Look for Plasmodium parasites.
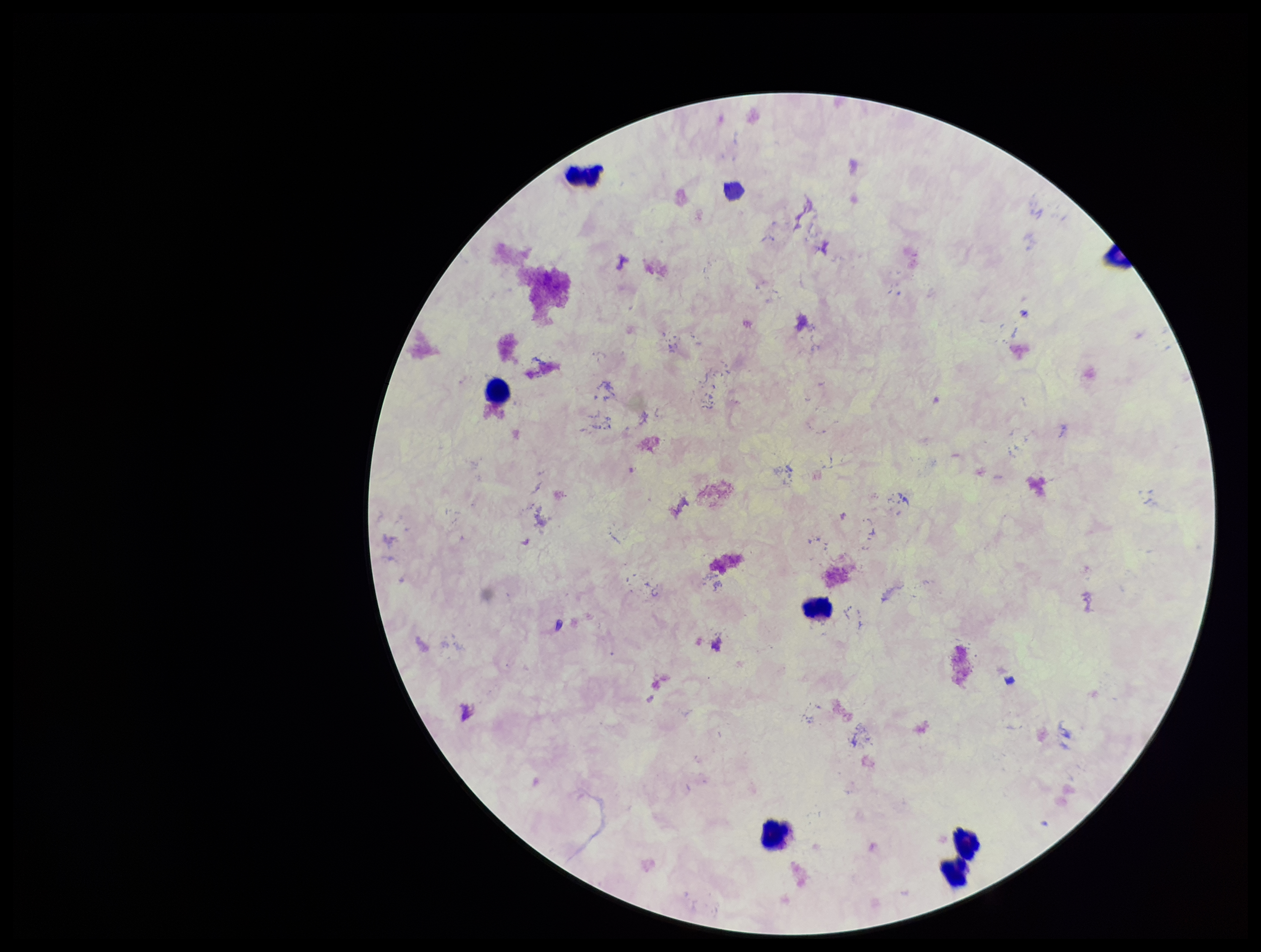
None detected.

capture: smartphone photograph through the microscope eyepiece
leukocyte_count: 7
field_of_view: single
parasite_count: 0
patient_malaria_status: negative
image_size: 1261×952 pixels
preparation: thick
stain: Giemsa